Identify the preparation type.
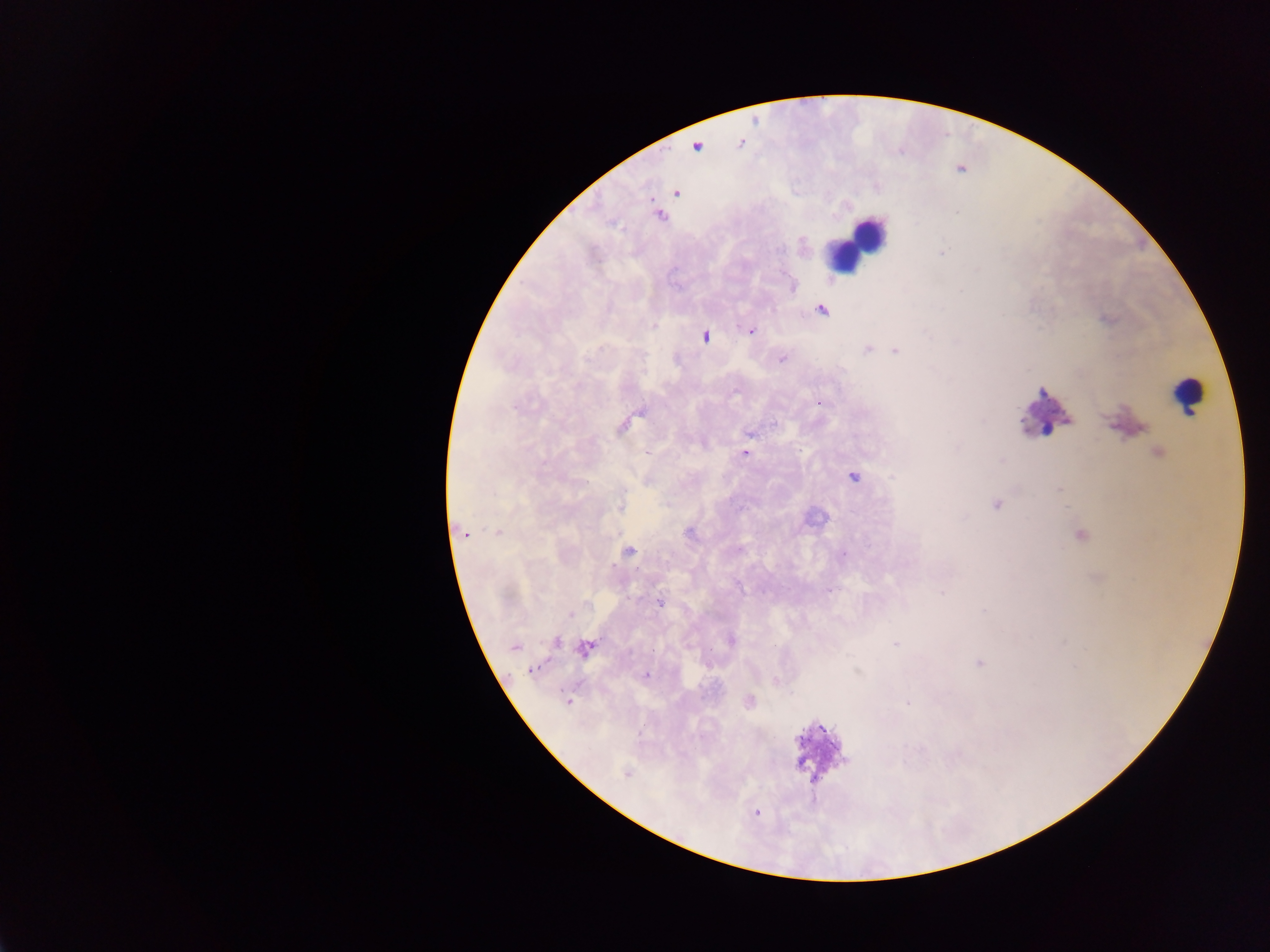
Thick blood smear.

image size = 1270×952 pixels
country = Ghana
leukocyte locations = approximate centers as (x, y) in pixels: (856, 243), (1188, 395)
malaria parasite locations = approximate centers as (x, y) in pixels: (741, 143), (696, 146), (676, 192), (659, 214), (821, 309), (751, 331), (704, 336), (869, 348), (894, 351), (782, 358), (819, 403), (625, 423), (749, 432), (744, 453), (1158, 453), (853, 476), (620, 504), (995, 504), (463, 531), (496, 532), (690, 533), (1079, 534), (627, 551), (828, 590), (659, 602), (731, 639), (557, 642), (514, 645), (585, 647), (980, 663), (535, 668), (645, 675), (775, 680), (749, 701), (567, 702), (627, 773), (757, 812)
capture = mobile-phone photograph through a microscope
field of view = single